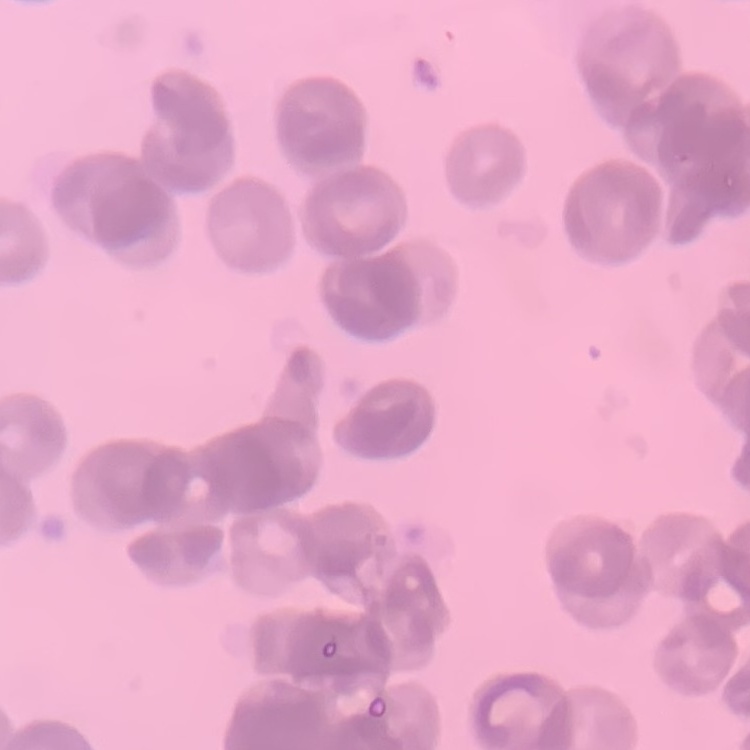

The erythrocytes exhibit rouleaux formation. Thin peripheral smear. One tile cut from a larger photomicrograph. Field's or Giemsa stain.